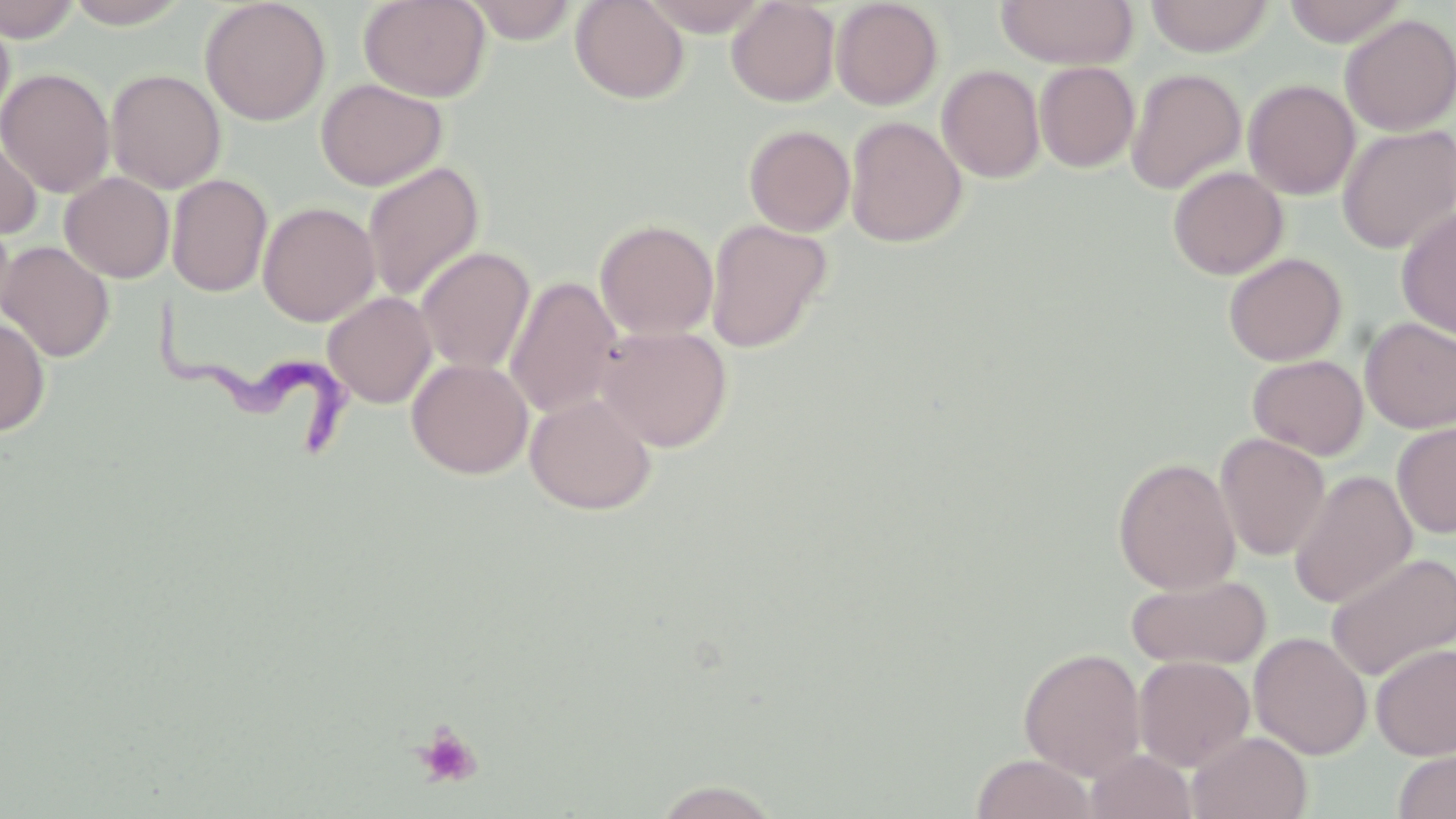
slide-level diagnosis = Trypanosoma brucei
field of view = single
uninfected red blood cell locations = approximate bounding boxes as named x1/y1/x2/y2 corners in pixels: (x1=0, y1=0, x2=83, y2=42), (x1=64, y1=0, x2=191, y2=28), (x1=359, y1=0, x2=491, y2=102), (x1=570, y1=0, x2=689, y2=104), (x1=640, y1=0, x2=772, y2=36), (x1=726, y1=0, x2=840, y2=107), (x1=996, y1=0, x2=1138, y2=69), (x1=1145, y1=0, x2=1274, y2=58), (x1=1282, y1=0, x2=1410, y2=46), (x1=200, y1=1, x2=331, y2=126), (x1=462, y1=1, x2=582, y2=43), (x1=831, y1=1, x2=944, y2=110), (x1=0, y1=11, x2=15, y2=134), (x1=1339, y1=14, x2=1456, y2=135), (x1=1034, y1=61, x2=1140, y2=173), (x1=937, y1=64, x2=1045, y2=183), (x1=1, y1=67, x2=115, y2=198), (x1=105, y1=68, x2=226, y2=193), (x1=1125, y1=68, x2=1246, y2=194), (x1=316, y1=78, x2=448, y2=191), (x1=1243, y1=79, x2=1360, y2=200), (x1=845, y1=116, x2=967, y2=247), (x1=743, y1=124, x2=855, y2=236), (x1=1337, y1=124, x2=1456, y2=253), (x1=0, y1=127, x2=42, y2=241), (x1=362, y1=161, x2=485, y2=303), (x1=1168, y1=166, x2=1288, y2=280), (x1=60, y1=172, x2=174, y2=283), (x1=167, y1=174, x2=273, y2=297), (x1=258, y1=202, x2=380, y2=326), (x1=1396, y1=206, x2=1456, y2=342), (x1=0, y1=214, x2=17, y2=331), (x1=595, y1=219, x2=719, y2=340), (x1=705, y1=219, x2=831, y2=352), (x1=0, y1=241, x2=114, y2=363), (x1=415, y1=246, x2=536, y2=375), (x1=1223, y1=252, x2=1348, y2=366), (x1=504, y1=276, x2=623, y2=419), (x1=322, y1=291, x2=437, y2=408), (x1=0, y1=317, x2=50, y2=436), (x1=1359, y1=317, x2=1456, y2=433), (x1=596, y1=325, x2=733, y2=452), (x1=1248, y1=354, x2=1368, y2=459), (x1=407, y1=357, x2=533, y2=479), (x1=525, y1=392, x2=656, y2=515), (x1=1392, y1=421, x2=1456, y2=539), (x1=1215, y1=433, x2=1330, y2=561), (x1=1113, y1=457, x2=1241, y2=594), (x1=1288, y1=470, x2=1417, y2=609), (x1=1325, y1=551, x2=1456, y2=680), (x1=1125, y1=573, x2=1271, y2=670), (x1=1249, y1=632, x2=1372, y2=760), (x1=1371, y1=643, x2=1456, y2=759), (x1=1019, y1=647, x2=1146, y2=781), (x1=1134, y1=656, x2=1255, y2=772), (x1=1188, y1=731, x2=1313, y2=818), (x1=1392, y1=748, x2=1456, y2=819), (x1=1086, y1=749, x2=1198, y2=819), (x1=970, y1=753, x2=1098, y2=819), (x1=653, y1=780, x2=781, y2=818)
preparation = thin blood film
modality = optical microscopy
Trypanosoma brucei locations = approximate bounding boxes as named x1/y1/x2/y2 corners in pixels: (x1=155, y1=295, x2=362, y2=448)
image size = 1456×819 pixels
stain = May-Grünwald-Giemsa
platelet locations = approximate bounding boxes as named x1/y1/x2/y2 corners in pixels: (x1=412, y1=723, x2=484, y2=790)
magnification = 1000x